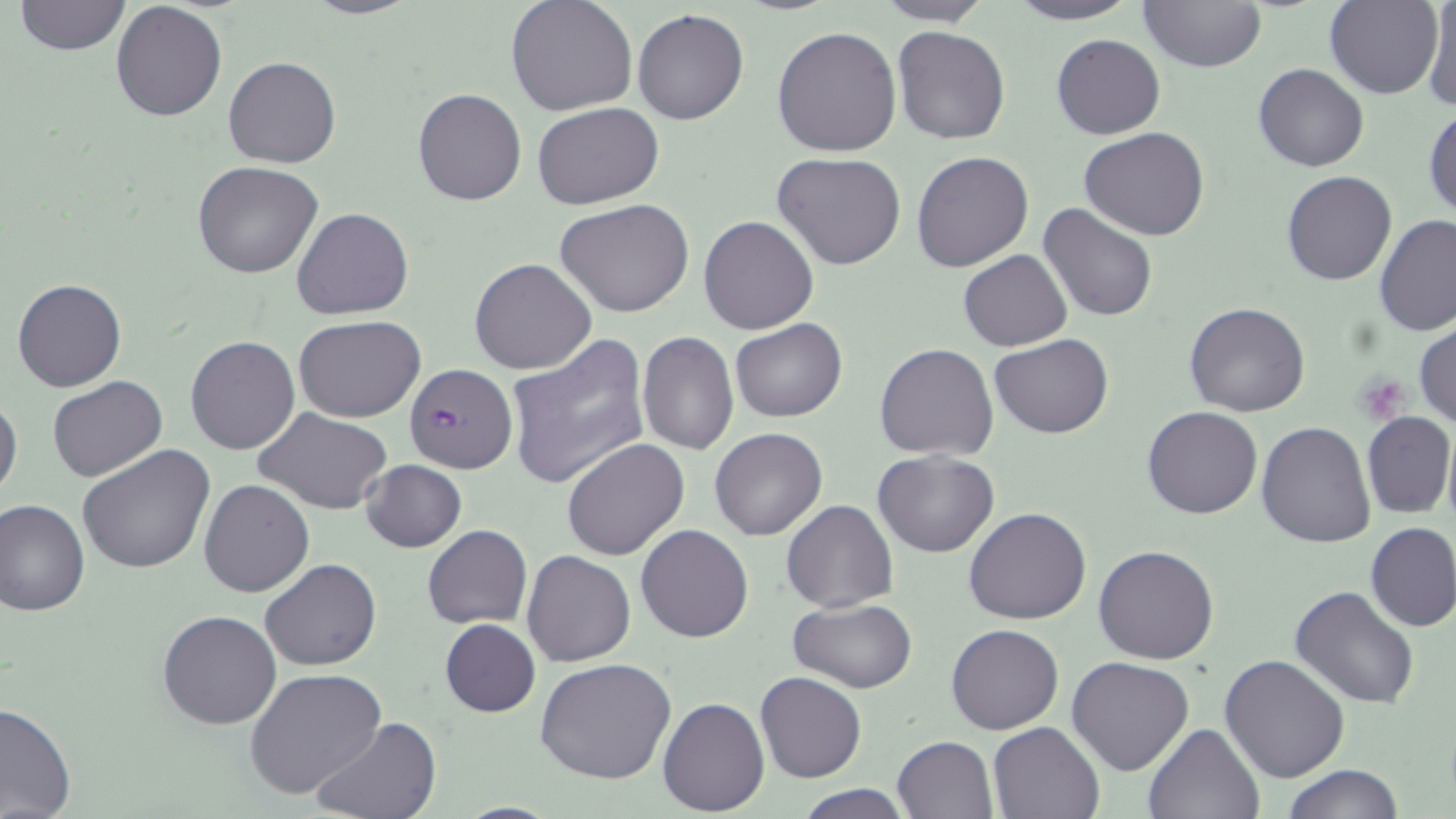
slide-level diagnosis = Plasmodium falciparum
stain = May-Grünwald-Giemsa
modality = optical microscopy
image size = 1456×819 pixels
preparation = thin blood smear
platelet locations = approximate bounding boxes as [x1, y1, x2, y2] in pixels: [1355, 373, 1410, 424]
magnification = 1000x
uninfected red blood cell locations = approximate bounding boxes as [x1, y1, x2, y2] in pixels: [299, 0, 422, 20], [505, 0, 637, 116], [872, 0, 995, 25], [1004, 0, 1139, 25], [1138, 0, 1266, 71], [1325, 0, 1442, 98], [1422, 0, 1456, 112], [15, 1, 130, 55], [110, 2, 227, 121], [633, 8, 749, 125], [771, 25, 902, 157], [893, 26, 1011, 145], [1051, 34, 1165, 140], [224, 56, 340, 168], [1253, 62, 1368, 172], [412, 87, 526, 207], [531, 102, 664, 209], [1423, 105, 1455, 225], [1081, 127, 1208, 241], [771, 151, 907, 270], [912, 151, 1034, 272], [193, 162, 324, 280], [1282, 171, 1397, 287], [556, 200, 695, 318], [1038, 202, 1160, 322], [293, 207, 413, 319], [1374, 214, 1456, 338], [698, 215, 819, 335], [958, 250, 1072, 351], [469, 258, 596, 375], [12, 277, 127, 392], [1184, 303, 1311, 417], [294, 316, 425, 421], [731, 318, 847, 421], [1413, 322, 1456, 430], [638, 332, 738, 456], [504, 333, 651, 490], [989, 335, 1114, 438], [185, 336, 301, 454], [875, 342, 998, 460], [48, 375, 166, 481], [0, 391, 23, 505], [1142, 405, 1263, 520], [252, 407, 393, 513], [1361, 411, 1454, 519], [1256, 423, 1376, 548], [1441, 424, 1456, 534], [709, 426, 828, 541], [562, 438, 690, 559], [78, 444, 215, 574], [872, 451, 1000, 557], [362, 459, 467, 552], [199, 479, 314, 597], [780, 497, 899, 613], [0, 499, 89, 618], [963, 507, 1092, 625], [636, 523, 754, 642], [1365, 523, 1456, 632], [423, 525, 532, 628], [1094, 544, 1220, 664], [520, 550, 635, 667], [261, 559, 381, 671], [1290, 587, 1421, 712], [789, 598, 917, 694], [157, 609, 283, 730], [440, 618, 541, 718], [946, 624, 1063, 734], [1220, 654, 1350, 783], [1066, 657, 1194, 775], [536, 658, 678, 785], [245, 667, 386, 800], [755, 671, 865, 783], [658, 696, 769, 816], [0, 701, 75, 819], [310, 716, 442, 819], [988, 720, 1105, 818], [1144, 722, 1265, 819], [891, 736, 997, 818], [1282, 765, 1404, 819], [793, 782, 912, 818]
field of view = one of a larger specimen
Plasmodium falciparum-infected red blood cell locations = approximate bounding boxes as [x1, y1, x2, y2] in pixels: [405, 363, 516, 473]